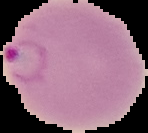

Image is 148×133 pixels. Cell region segmented out of the field of view; the surrounding area is masked to black. From a thin blood film. Result: malaria parasites identified.